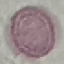

result = no malaria parasites detected
preparation = thin blood smear
image type = automatically extracted cell patch, resized to 64 × 64 pixels
stain = Giemsa
capture = smartphone camera at the microscope eyepiece